Give the extent of all Plasmodium ovale-infected red blood cells.
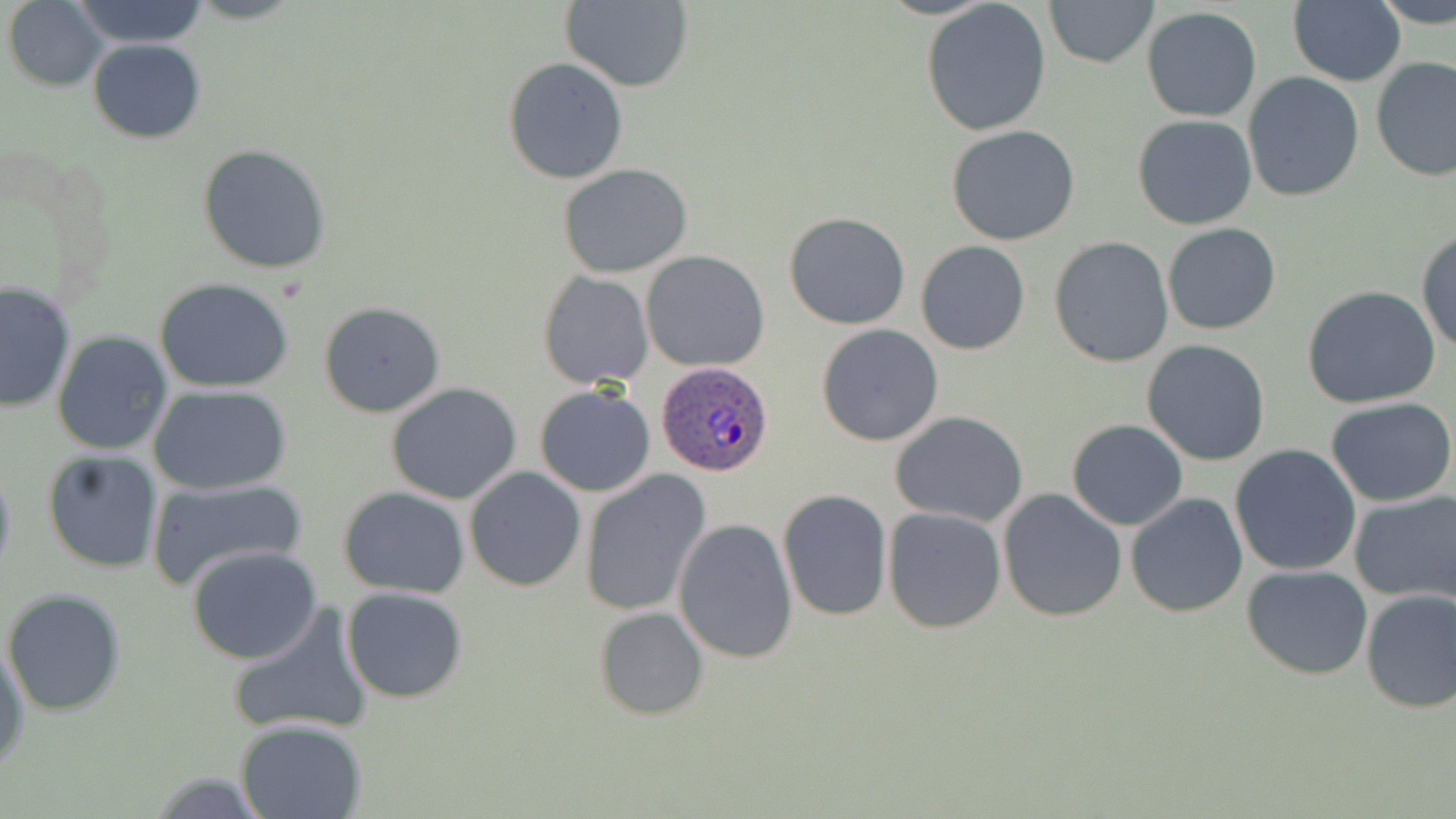
Approximate bounding boxes as (x1, y1, x2, y2) in pixels.
Plasmodium ovale-infected red blood cells: (656, 363, 773, 478).

Summary:
  - Uninfected red blood cell locations: (67, 0, 214, 48), (1043, 0, 1158, 70), (1375, 0, 1456, 29), (4, 1, 107, 90), (559, 1, 694, 92), (921, 1, 1053, 137), (1287, 2, 1406, 86), (1141, 6, 1262, 123), (88, 38, 206, 143), (504, 57, 628, 183), (1372, 57, 1456, 184), (1243, 74, 1365, 204), (1132, 115, 1258, 229), (945, 126, 1081, 246), (197, 144, 333, 273), (558, 162, 694, 277), (783, 211, 911, 330), (1162, 222, 1281, 336), (1417, 226, 1456, 356), (1048, 236, 1174, 367), (916, 240, 1030, 355), (642, 250, 769, 371), (538, 271, 653, 388), (154, 277, 297, 390), (1, 281, 76, 414), (1302, 285, 1440, 409), (320, 302, 446, 418), (816, 324, 944, 447), (52, 331, 173, 455), (1141, 339, 1272, 466), (388, 382, 522, 503), (149, 384, 293, 495), (533, 385, 655, 497), (1326, 397, 1456, 507), (890, 412, 1028, 526), (1066, 420, 1188, 531), (1230, 443, 1363, 577), (41, 449, 163, 574), (0, 460, 16, 583), (464, 467, 586, 591), (581, 472, 712, 616), (146, 474, 307, 589), (338, 486, 470, 599), (998, 488, 1128, 622), (778, 490, 891, 622), (1347, 490, 1456, 603), (1126, 491, 1248, 618), (882, 507, 1005, 633), (673, 517, 799, 661), (186, 546, 326, 665), (1241, 565, 1372, 680), (341, 587, 468, 702), (3, 588, 127, 716), (1359, 588, 1456, 712), (223, 601, 374, 741), (594, 606, 709, 721), (1, 645, 29, 773), (235, 720, 368, 818)
  - Slide-level diagnosis: Plasmodium ovale
  - Preparation: thin blood smear
  - Modality: optical microscopy
  - Magnification: 1000x
  - Stain: May-Grünwald-Giemsa
  - Field of view: one of a larger specimen
  - Image size: 1456×819 pixels